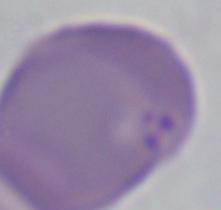
identification = Babesia
magnification = 1000x
modality = photomicrograph